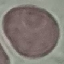 Result: no malaria parasites seen. Automatically extracted cell patch, resized to 64 × 64 pixels. Giemsa-stained preparation. Photographed with a smartphone camera at the microscope eyepiece. Thin blood smear.